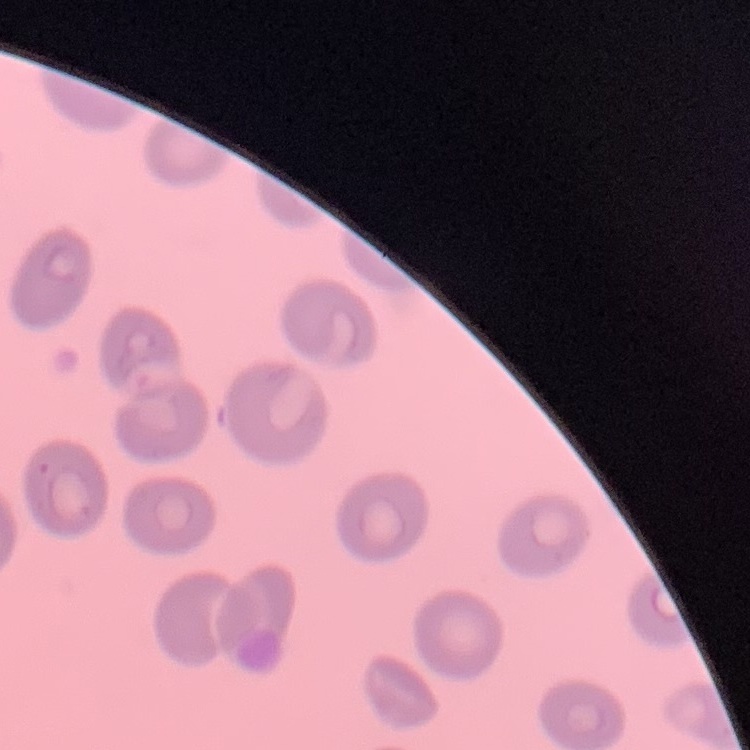
Summary:
  - Red blood cell morphology: no rouleaux formation
  - Stain: Field's or Giemsa
  - Image type: one tile cut from a larger photomicrograph
  - Preparation: thin blood film